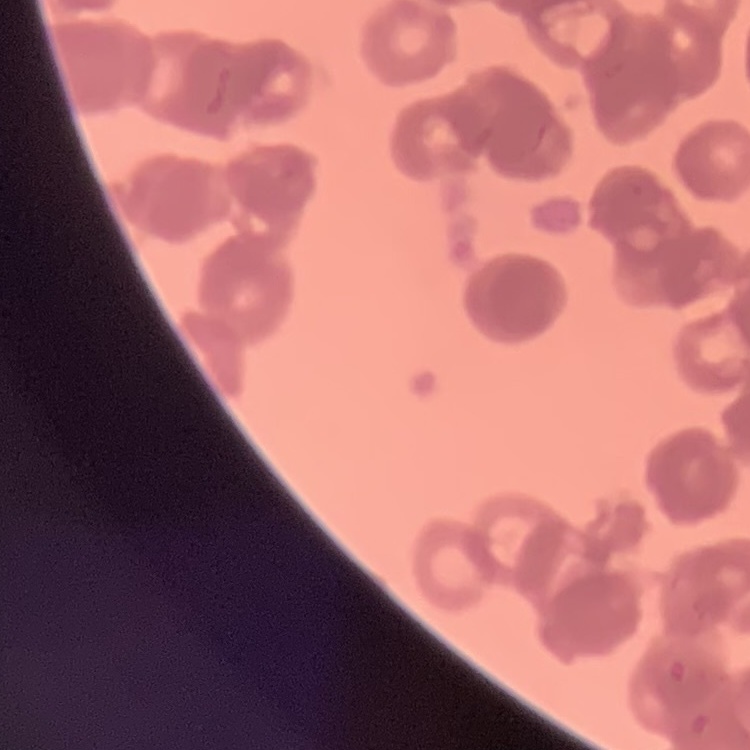 The erythrocytes show rouleaux formation. Square crop of a larger photomicrograph. Thin blood smear. Stained with either Field's or Giemsa.